Report the malaria status of this cell.
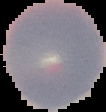
Uninfected.

image_size: 106×112 pixels
preparation: thin blood film
image_type: cell region segmented out of the field of view; surrounding area masked to black